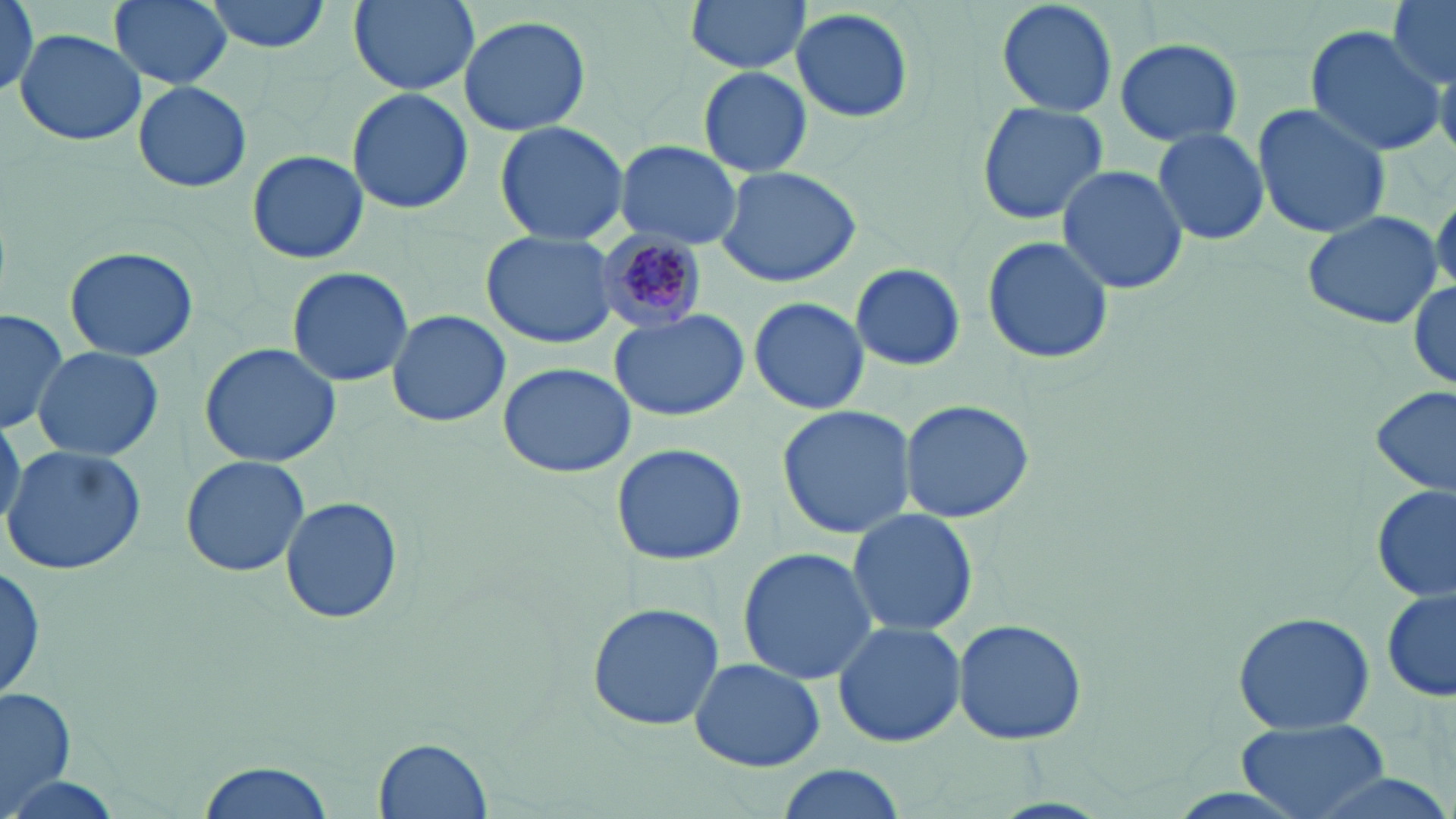
Approximate bounding boxes as [x1, y1, x2, y2] in pixels. Uninfected red blood cell locations: [109, 0, 232, 89], [201, 0, 334, 52], [345, 0, 481, 95], [683, 0, 807, 77], [993, 0, 1119, 117], [1386, 0, 1455, 86], [0, 1, 43, 91], [789, 7, 915, 124], [459, 14, 592, 135], [1304, 24, 1445, 159], [14, 29, 148, 147], [1113, 37, 1243, 148], [698, 67, 812, 178], [132, 80, 252, 193], [346, 88, 474, 213], [976, 101, 1109, 226], [1249, 101, 1392, 241], [494, 119, 630, 243], [1151, 126, 1270, 247], [615, 140, 742, 247], [247, 148, 369, 265], [717, 164, 864, 287], [1056, 165, 1188, 295], [1428, 186, 1456, 303], [1300, 209, 1444, 331], [482, 232, 620, 349], [980, 235, 1113, 366], [64, 246, 198, 360], [850, 262, 965, 372], [285, 265, 414, 388], [1409, 278, 1456, 390], [749, 296, 870, 416], [0, 308, 69, 435], [386, 308, 511, 426], [610, 310, 748, 421], [198, 342, 341, 466], [31, 345, 163, 461], [497, 362, 638, 478], [1372, 384, 1455, 499], [900, 398, 1033, 524], [776, 403, 919, 540], [0, 417, 24, 530], [610, 441, 748, 566], [2, 446, 149, 576], [180, 455, 310, 577], [1373, 483, 1454, 605], [277, 492, 405, 628], [845, 506, 979, 638], [737, 546, 880, 685], [0, 554, 46, 706], [1381, 588, 1455, 706], [584, 602, 726, 730], [1231, 609, 1374, 734], [952, 618, 1087, 746], [832, 620, 966, 749], [688, 657, 825, 772], [0, 684, 79, 812], [1235, 717, 1389, 818], [375, 736, 494, 819], [192, 762, 334, 819], [774, 763, 909, 819], [1290, 767, 1456, 819]. Plasmodium malariae-infected red blood cell locations: [594, 227, 707, 334]. Slide-level diagnosis: Plasmodium malariae. Thin blood film. Single field of view. Image is 1456×819 pixels. Captured at 1000x magnification. May-Grünwald-Giemsa-stained preparation. Light microscopy.